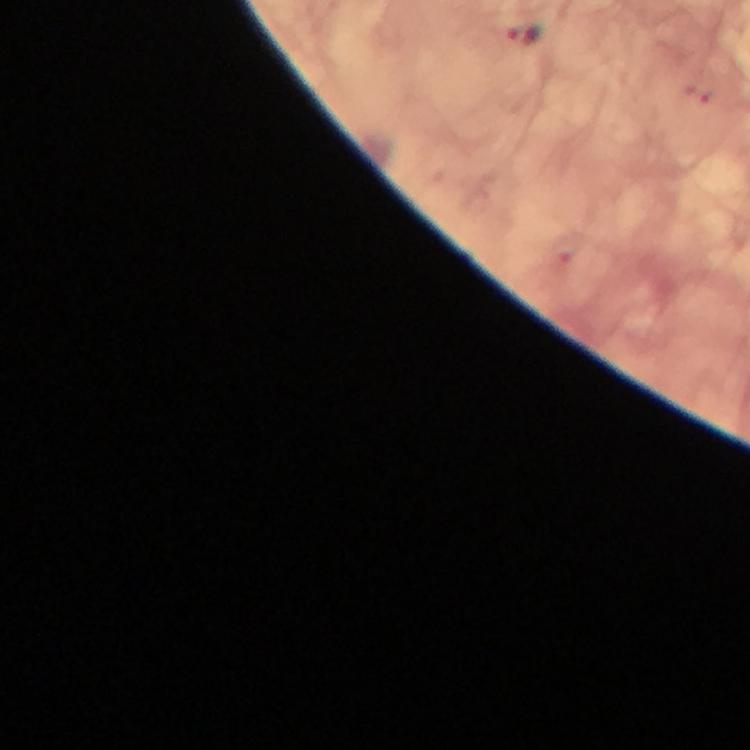 Approximate centers as (x, y) in pixels. Malaria parasite locations: (522, 33). 100x magnification. From a malaria diagnostic workup. Giemsa-stained preparation. Cropped region of a single field of view. Image is 750×750 pixels. Photographed with a smartphone mounted on the microscope. Immersion oil applied. Thick blood smear.